Locate every blood parasite and identify its species.
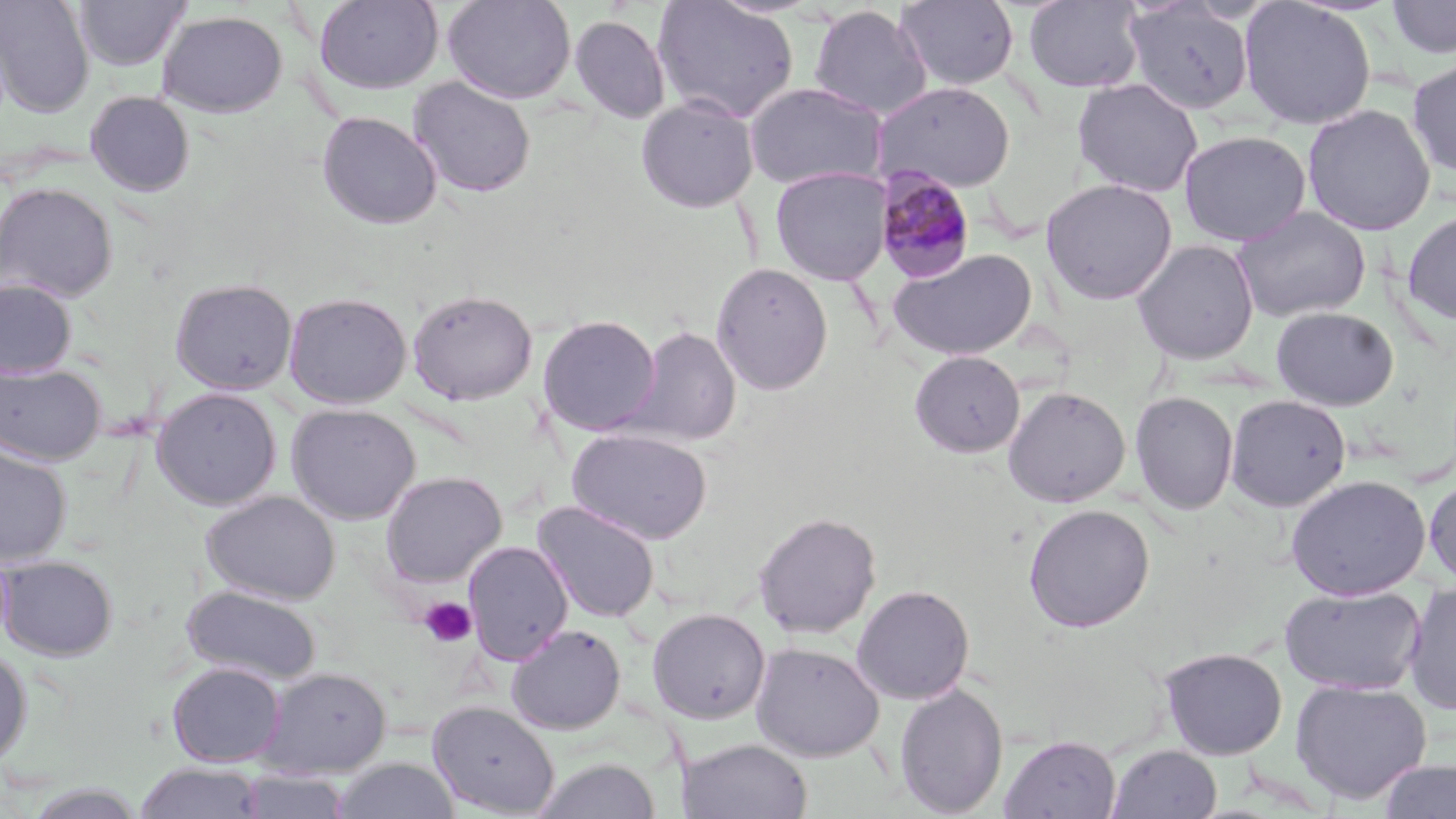
Approximate bounding boxes as [x1, y1, x2, y2] in pixels.
Plasmodium malariae-infected red blood cells: [875, 165, 978, 283].
No Plasmodium falciparum, Plasmodium ovale, Plasmodium vivax, Babesia divergens, or Trypanosoma brucei observed.

Summary:
  - Platelet locations: [418, 597, 477, 649]
  - Uninfected red blood cell locations: [0, 0, 94, 118], [73, 0, 191, 72], [314, 0, 443, 94], [442, 0, 577, 104], [652, 0, 801, 124], [894, 0, 1020, 91], [1022, 0, 1147, 93], [1386, 0, 1456, 59], [1123, 1, 1256, 115], [1238, 1, 1376, 130], [808, 5, 931, 120], [157, 10, 288, 118], [568, 15, 671, 125], [1406, 58, 1456, 178], [408, 76, 536, 199], [1072, 78, 1203, 197], [745, 82, 887, 191], [873, 82, 1016, 192], [85, 90, 195, 197], [636, 94, 759, 213], [1302, 104, 1436, 236], [316, 111, 442, 229], [1179, 130, 1311, 246], [770, 166, 891, 286], [1040, 178, 1178, 305], [1, 182, 118, 303], [1231, 206, 1371, 323], [1402, 209, 1456, 324], [1132, 240, 1259, 364], [887, 248, 1038, 360], [710, 261, 834, 396], [0, 278, 77, 379], [169, 278, 298, 395], [407, 288, 539, 405], [283, 291, 412, 409], [1271, 306, 1399, 411], [538, 314, 661, 436], [626, 325, 741, 448], [909, 350, 1026, 457], [0, 361, 106, 466], [1003, 386, 1131, 507], [151, 387, 282, 510], [1130, 391, 1238, 516], [1225, 394, 1351, 511], [286, 403, 421, 525], [567, 428, 713, 544], [0, 442, 72, 566], [379, 471, 507, 588], [1286, 474, 1430, 600], [1423, 475, 1456, 588], [200, 490, 340, 605], [532, 500, 661, 623], [1023, 504, 1155, 633], [753, 511, 881, 639], [463, 540, 574, 665], [1, 555, 118, 661], [1403, 581, 1456, 715], [851, 584, 975, 705], [1280, 584, 1426, 695], [181, 585, 321, 685], [648, 608, 770, 724], [506, 623, 627, 734], [750, 642, 884, 762], [1159, 646, 1288, 760], [0, 647, 32, 769], [166, 661, 287, 767], [256, 666, 392, 779], [1290, 678, 1432, 804], [893, 682, 1009, 817], [427, 700, 559, 817], [999, 734, 1121, 819], [679, 738, 813, 819], [1106, 744, 1223, 819], [331, 757, 459, 819], [532, 757, 661, 819], [1376, 759, 1456, 818], [134, 762, 265, 819], [236, 770, 352, 818], [22, 782, 146, 818]
  - Slide-level diagnosis: Plasmodium malariae
  - Stain: May-Grünwald-Giemsa
  - Modality: optical microscopy
  - Preparation: thin blood smear
  - Magnification: 1000x
  - Field of view: one of a larger specimen
  - Image size: 1456×819 pixels